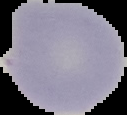

preparation = thin blood smear
image size = 127×115 pixels
image type = cell region segmented out of the field of view; surrounding area masked to black
result = negative for malaria parasites